Report the malaria status of this cell.
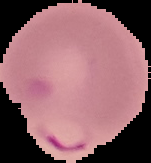
Parasitized.

Summary:
  - Image size: 151×163 pixels
  - Image type: segmented cell region on a black background
  - Preparation: thin blood film